Report the malaria status of this cell.
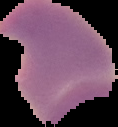

It is parasitized.

Segmented cell region on a black background. Image is 118×127 pixels. From a thin blood film.